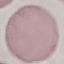

Summary:
  - Malaria status: uninfected
  - Capture: smartphone camera at the microscope eyepiece
  - Preparation: thin smear
  - Image type: automatically extracted cell patch, resized to 64 × 64 pixels
  - Stain: Giemsa